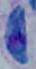

Summary:
  - Magnification: 1000x
  - Modality: micrograph
  - Identification: Toxoplasma gondii